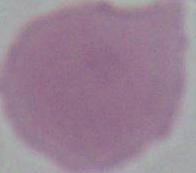

Captured at 1000x magnification. Photomicrograph. An erythrocyte is seen.